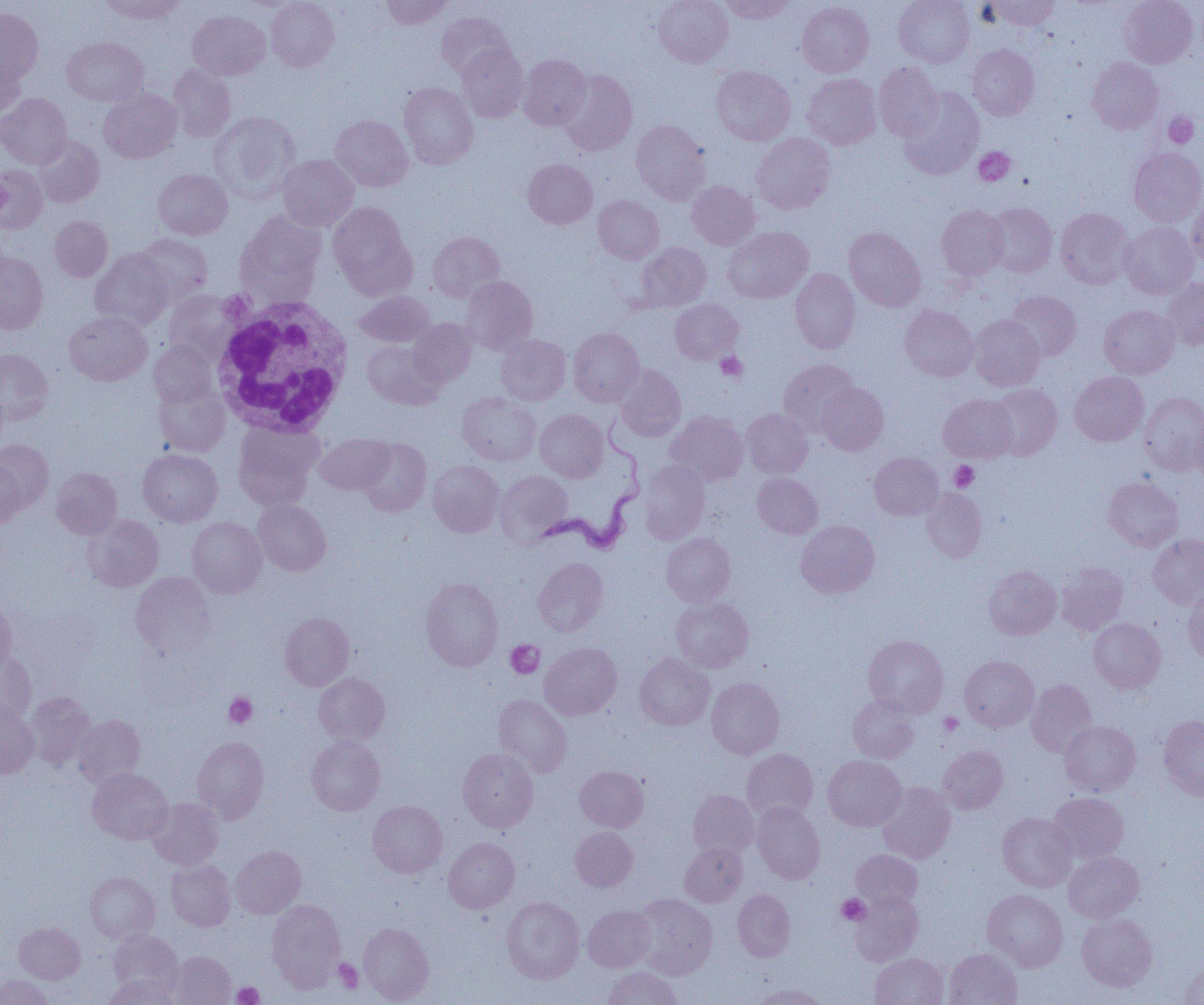

slide-level diagnosis = Trypanosoma brucei
uninfected red blood cell locations = approximate bounding boxes as [x1, y1, x2, y2] in pixels: [99, 0, 184, 24], [266, 0, 339, 71], [381, 0, 452, 29], [654, 0, 733, 67], [720, 0, 795, 24], [894, 0, 974, 67], [983, 0, 1059, 31], [1120, 0, 1198, 67], [797, 1, 874, 77], [0, 8, 43, 85], [188, 10, 270, 80], [435, 11, 514, 79], [63, 37, 148, 107], [457, 44, 529, 122], [967, 44, 1039, 119], [0, 52, 25, 121], [519, 54, 591, 129], [1087, 57, 1163, 133], [874, 62, 943, 141], [168, 64, 236, 142], [711, 66, 795, 145], [558, 70, 637, 156], [803, 73, 881, 149], [398, 82, 478, 169], [899, 87, 983, 179], [98, 89, 182, 164], [0, 93, 71, 168], [209, 111, 300, 201], [330, 115, 413, 191], [631, 120, 711, 204], [751, 132, 835, 214], [33, 135, 105, 207], [1129, 148, 1204, 226], [277, 155, 358, 231], [523, 159, 597, 229], [0, 164, 48, 234], [153, 169, 233, 239], [687, 181, 760, 250], [593, 195, 664, 263], [1186, 198, 1204, 267], [328, 202, 415, 294], [986, 203, 1057, 277], [936, 205, 1008, 280], [1055, 207, 1134, 289], [235, 210, 325, 303], [50, 216, 113, 281], [1119, 221, 1199, 299], [723, 227, 813, 303], [844, 227, 926, 312], [428, 231, 505, 302], [136, 234, 212, 305], [636, 242, 711, 311], [90, 249, 173, 330], [0, 251, 48, 334], [790, 268, 860, 353], [462, 276, 538, 354], [1162, 277, 1204, 349], [164, 290, 242, 361], [1006, 290, 1081, 361], [354, 291, 435, 347], [670, 299, 743, 364], [900, 304, 978, 382], [1099, 305, 1180, 379], [64, 311, 152, 386], [969, 314, 1045, 391], [408, 318, 477, 387], [568, 327, 644, 406], [496, 334, 571, 405], [362, 340, 442, 409], [149, 341, 219, 407], [0, 349, 53, 424], [779, 359, 858, 435], [614, 364, 686, 441], [1070, 372, 1148, 446], [154, 383, 230, 457], [816, 383, 889, 455], [987, 383, 1062, 459], [0, 385, 10, 451], [457, 392, 541, 466], [1139, 392, 1204, 475], [939, 394, 1018, 463], [536, 409, 608, 482], [741, 409, 813, 478], [666, 411, 748, 485], [1190, 414, 1204, 484], [233, 422, 324, 508], [316, 433, 394, 494], [357, 438, 431, 517], [0, 440, 54, 514], [137, 448, 223, 527], [870, 452, 943, 520], [0, 459, 25, 530], [428, 460, 504, 537], [639, 460, 710, 544], [51, 467, 122, 539], [496, 471, 573, 545], [753, 473, 823, 538], [1103, 476, 1183, 551], [921, 488, 986, 563], [252, 499, 331, 575], [83, 514, 164, 591], [187, 517, 266, 598], [796, 520, 879, 598], [662, 533, 735, 606], [1148, 533, 1204, 609], [532, 557, 609, 636], [1056, 562, 1128, 635], [983, 565, 1061, 639], [131, 572, 216, 659], [420, 577, 503, 671], [1183, 590, 1204, 665], [671, 597, 754, 672], [0, 599, 17, 673], [279, 611, 354, 690], [1088, 618, 1165, 693], [863, 635, 949, 717], [539, 642, 622, 720], [0, 651, 37, 725], [635, 653, 715, 730], [960, 655, 1039, 731], [314, 673, 390, 745], [706, 678, 784, 759], [1027, 679, 1097, 757], [24, 691, 96, 770], [493, 694, 572, 776], [846, 694, 920, 763], [0, 700, 39, 779], [73, 714, 145, 788], [1158, 715, 1204, 801], [1060, 720, 1141, 795], [192, 736, 269, 823], [306, 736, 385, 815], [938, 746, 1008, 814], [457, 748, 538, 831], [741, 748, 818, 822], [823, 755, 906, 831], [575, 766, 649, 832], [87, 768, 173, 845], [877, 782, 956, 864], [688, 790, 759, 859], [1048, 792, 1129, 863], [147, 798, 224, 869], [367, 800, 447, 878], [752, 802, 825, 884], [997, 812, 1078, 891], [570, 827, 638, 892], [443, 837, 519, 913], [680, 842, 747, 906], [231, 845, 306, 918], [851, 849, 922, 909], [1063, 851, 1143, 922], [166, 859, 235, 931], [85, 872, 160, 943], [732, 889, 795, 962], [983, 889, 1068, 971], [850, 890, 923, 965], [632, 894, 717, 980], [501, 897, 584, 983], [266, 899, 345, 990], [583, 905, 656, 971], [1077, 914, 1157, 990], [14, 922, 85, 983], [358, 922, 434, 1004], [107, 929, 184, 994], [944, 948, 1022, 1005], [170, 951, 235, 1004], [869, 953, 948, 1005], [1180, 962, 1204, 1004], [602, 967, 682, 1005], [104, 974, 180, 1005], [0, 975, 53, 1005], [753, 983, 830, 1005]
white blood cell locations = approximate bounding boxes as [x1, y1, x2, y2] in pixels: [209, 295, 355, 436]
platelet locations = approximate bounding boxes as [x1, y1, x2, y2] in pixels: [1163, 113, 1200, 149], [973, 147, 1015, 186], [0, 168, 10, 228], [716, 352, 747, 381], [949, 461, 978, 491], [506, 640, 544, 678], [224, 692, 257, 728], [938, 713, 963, 736], [836, 894, 870, 925], [333, 959, 363, 994], [233, 981, 264, 1005]
field of view = one of a larger specimen
preparation = thin blood smear
Trypanosoma brucei locations = approximate bounding boxes as [x1, y1, x2, y2] in pixels: [534, 425, 646, 555]
modality = optical microscopy
image size = 1204×1005 pixels
magnification = 1000x